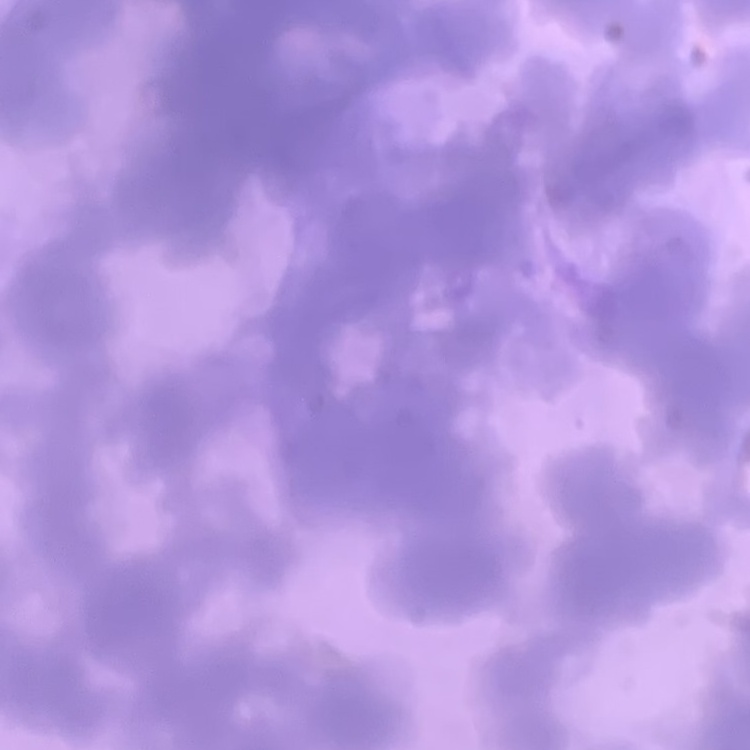
Summary:
  - Red blood cell morphology: rouleaux formation
  - Stain: Field's or Giemsa
  - Preparation: thin blood smear
  - Image type: square crop of a larger photomicrograph